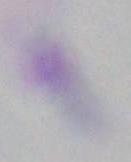 1000x magnification. Toxoplasma gondii is seen. Photomicrograph.